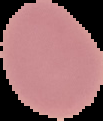 From a thin blood smear. The area outside the segmented cell region is set to black. Malaria status: uninfected. Image is 103×121 pixels.